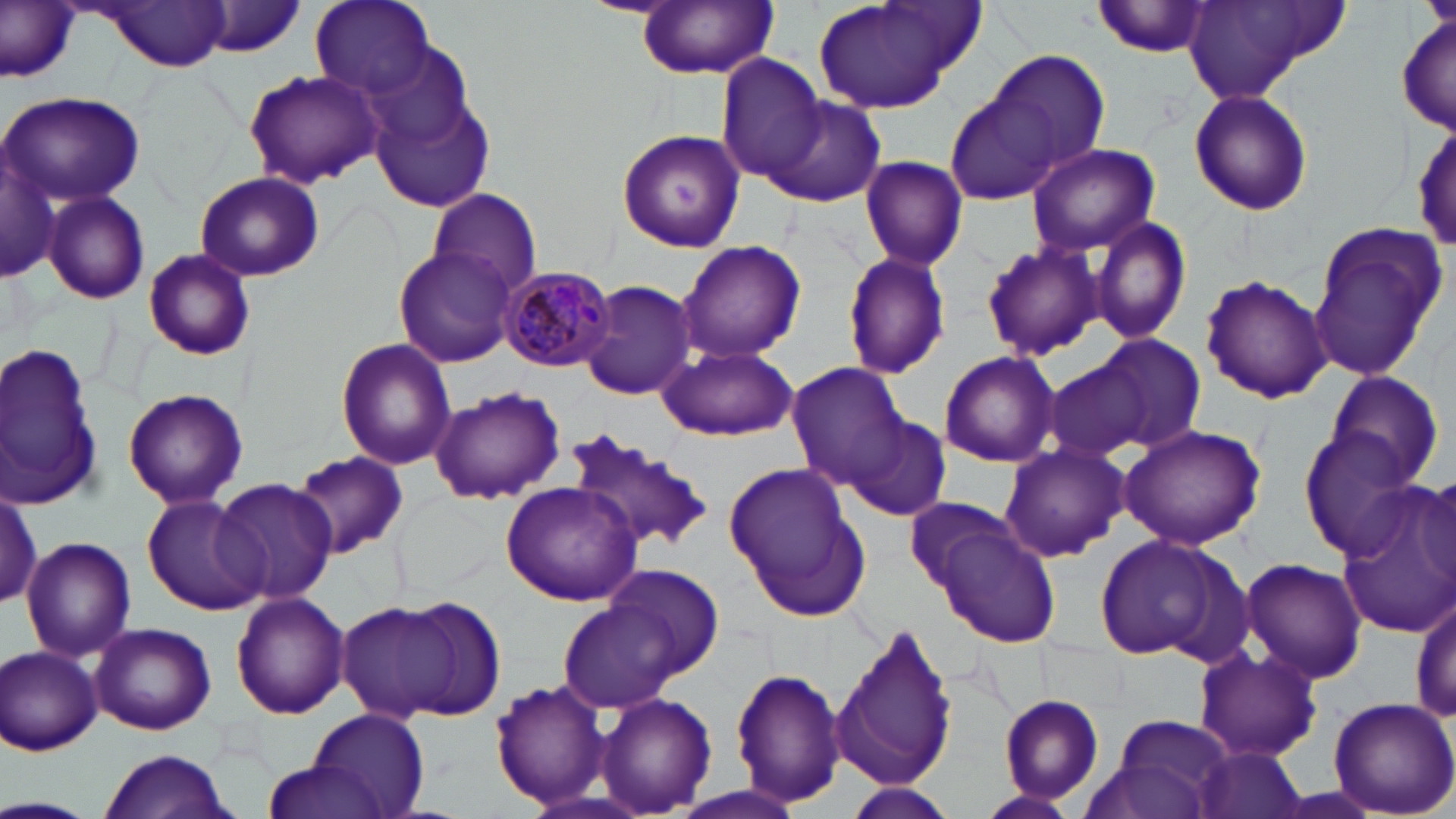

{
  "slide_level_diagnosis": "Plasmodium malariae",
  "field_of_view": "single",
  "stain": "May-Grünwald-Giemsa",
  "image_size": "1456×819 pixels",
  "modality": "light microscopy",
  "preparation": "thin blood film",
  "plasmodium_malariae_infected_red_blood_cell_locations": "approximate bounding boxes as (x1,y1)-(x2,y2) corner pairs in pixels: (500,265)-(618,372)",
  "magnification": "1000x",
  "uninfected_red_blood_cell_locations": "approximate bounding boxes as (x1,y1)-(x2,y2) corner pairs in pixels: (1,0)-(83,81), (310,0)-(435,96), (811,0)-(978,117), (637,1)-(780,77), (1094,1)-(1216,58), (1182,1)-(1342,106), (96,2)-(233,70), (196,2)-(309,58), (1396,9)-(1454,137), (985,48)-(1111,173), (717,56)-(829,183), (242,69)-(383,189), (370,85)-(496,213), (1188,89)-(1314,216), (1,91)-(148,207), (945,95)-(1063,207), (764,97)-(884,208), (1411,118)-(1454,252), (617,128)-(745,253), (1027,142)-(1161,255), (2,150)-(59,282), (860,155)-(969,272), (194,171)-(325,282), (428,188)-(544,296), (41,191)-(150,306), (1090,212)-(1193,344), (1308,223)-(1445,383), (678,239)-(806,361), (981,240)-(1103,361), (392,243)-(516,368), (143,249)-(256,359), (842,250)-(951,381), (1201,274)-(1331,403), (580,279)-(698,401), (1089,333)-(1207,453), (335,338)-(456,469), (0,341)-(107,513), (658,345)-(798,440), (938,352)-(1060,467), (1042,354)-(1157,463), (785,362)-(910,488), (1323,370)-(1445,490), (122,386)-(249,509), (431,387)-(565,505), (843,414)-(951,521), (1118,423)-(1267,551), (567,428)-(718,556), (1297,430)-(1423,561), (998,443)-(1131,562), (293,450)-(409,558), (721,463)-(860,604), (213,477)-(339,607), (502,480)-(645,605), (1,484)-(43,611), (1329,486)-(1456,637), (142,495)-(265,617), (902,495)-(1018,594), (930,519)-(1060,649), (1093,534)-(1239,663), (20,535)-(137,660), (1238,556)-(1368,686), (604,561)-(724,682), (229,592)-(350,720), (1411,594)-(1455,726), (392,595)-(508,720), (558,596)-(691,712), (336,601)-(459,721), (832,618)-(957,794), (89,622)-(216,735), (3,645)-(102,755), (1194,647)-(1322,762), (732,666)-(847,807), (488,677)-(612,812), (593,691)-(717,817), (998,695)-(1104,803), (1326,696)-(1456,819), (307,709)-(429,818), (1106,713)-(1238,816), (1195,748)-(1307,819), (98,750)-(233,818), (257,758)-(389,819), (844,784)-(956,819), (978,791)-(1079,816), (0,796)-(94,818)"
}